Report the malaria status of this cell.
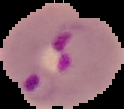

It is parasitized.

Segmented cell region on a black background. From a thin blood smear. Image is 124×109 pixels.